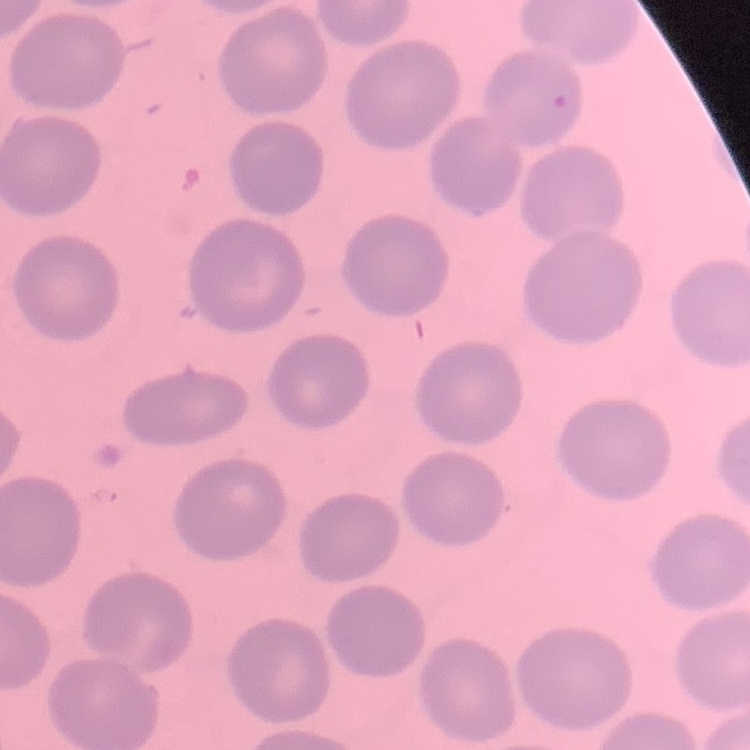

Summary:
  - Red blood cell morphology: no rouleaux formation
  - Image type: one tile cut from a larger photomicrograph
  - Preparation: thin peripheral smear
  - Stain: Field's or Giemsa